Locate every leukocyte (white blood cell).
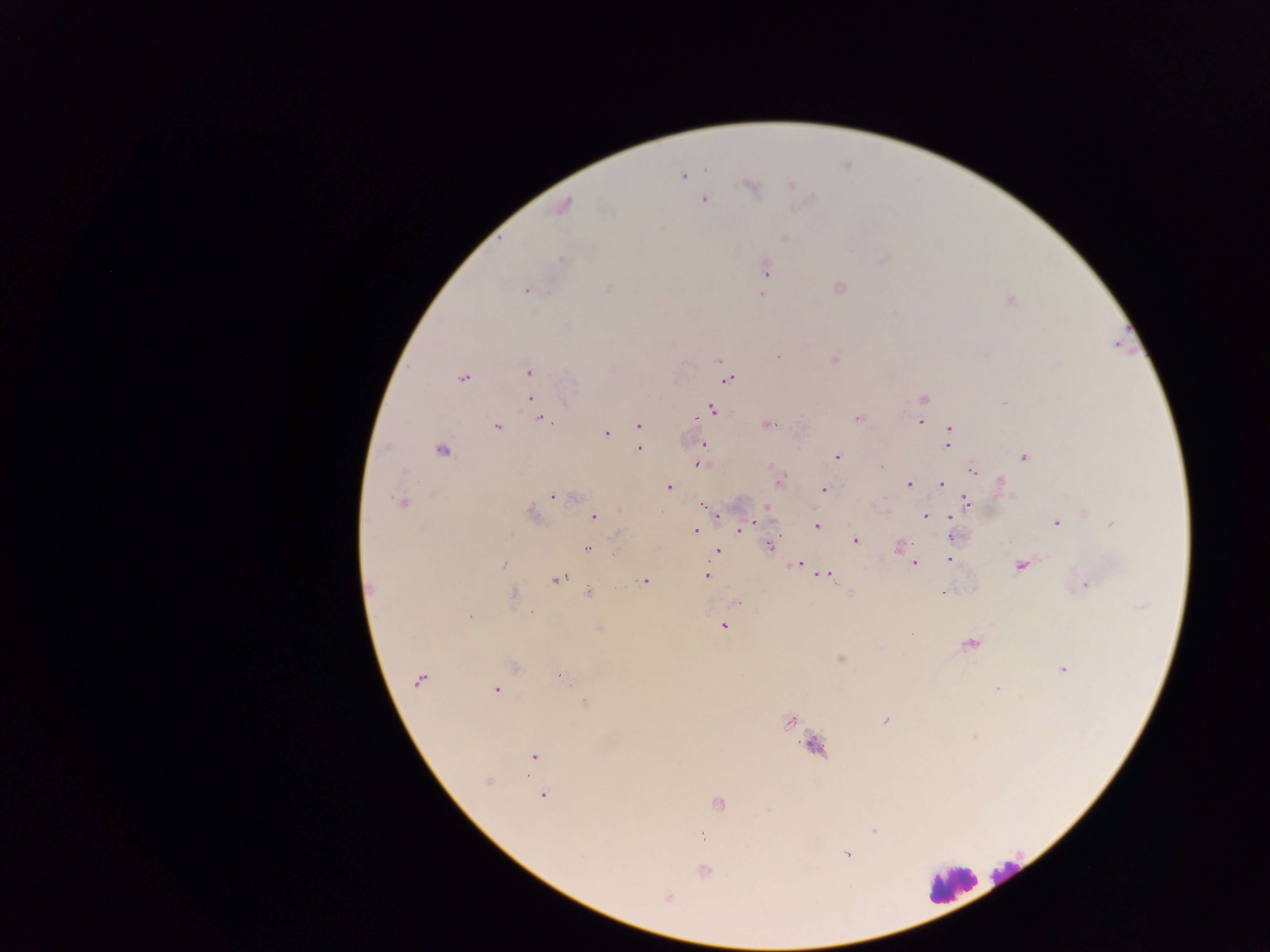

Approximate centers as [x, y] in pixels.
Leukocytes: [1013, 873], [951, 884].

{
  "malaria_parasite_locations": "approximate centers as [x, y] in pixels: [706, 170], [684, 175], [791, 185], [752, 187], [704, 200], [564, 205], [785, 237], [561, 259], [766, 269], [839, 287], [608, 289], [526, 290], [761, 294], [1010, 301], [565, 325], [777, 357], [834, 359], [719, 361], [528, 372], [463, 378], [727, 378], [530, 399], [923, 399], [1003, 402], [533, 404], [712, 409], [541, 418], [858, 419], [920, 422], [768, 424], [639, 426], [496, 428], [949, 430], [606, 433], [703, 444], [948, 444], [387, 446], [640, 448], [442, 451], [702, 452], [837, 457], [1024, 457], [699, 464], [881, 467], [973, 471], [780, 480], [1001, 481], [909, 484], [942, 484], [669, 487], [823, 489], [552, 497], [401, 502], [967, 502], [704, 507], [768, 507], [619, 510], [531, 513], [717, 515], [926, 516], [593, 517], [950, 517], [1056, 523], [1112, 524], [816, 525], [740, 530], [695, 531], [620, 533], [950, 536], [855, 541], [770, 546], [898, 546], [588, 548], [717, 551], [949, 560], [503, 564], [913, 564], [797, 565], [1020, 566], [826, 575], [707, 576], [558, 579], [644, 581], [1086, 585], [942, 592], [589, 593], [512, 595], [1141, 607], [470, 617], [723, 627], [599, 628], [969, 645], [841, 658], [513, 667], [1063, 669], [561, 676], [419, 680], [997, 688], [495, 689], [585, 703], [886, 720], [789, 723], [815, 748], [534, 756], [488, 780], [543, 795], [718, 804], [768, 810], [874, 831], [702, 836], [848, 855], [581, 857], [704, 871], [668, 896]",
  "image_size": "1270×952 pixels",
  "country": "Ghana",
  "field_of_view": "single",
  "capture": "mobile-phone photograph through a microscope",
  "preparation": "thick blood film"
}